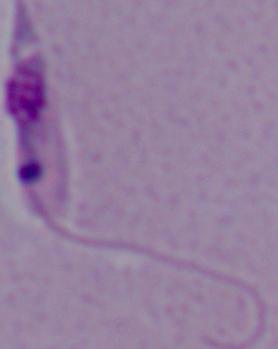
A Leishmania parasite is seen. 1000x magnification. Micrograph.